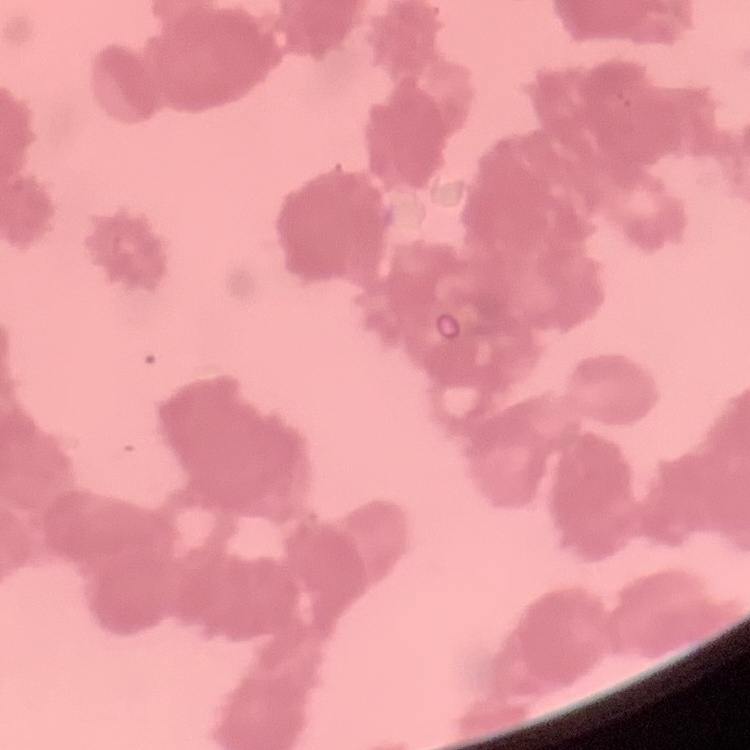

Summary:
  - Red blood cell morphology: rouleaux formation
  - Preparation: thin blood film
  - Image type: square crop of a larger photomicrograph
  - Stain: Field's or Giemsa